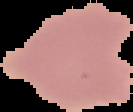 Result: no Plasmodium parasites detected. Image is 133×112 pixels. From a thin blood film. Cell region segmented out of the field of view; the surrounding area is masked to black.